Give the position of every Plasmodium parasite and every leukocyte.
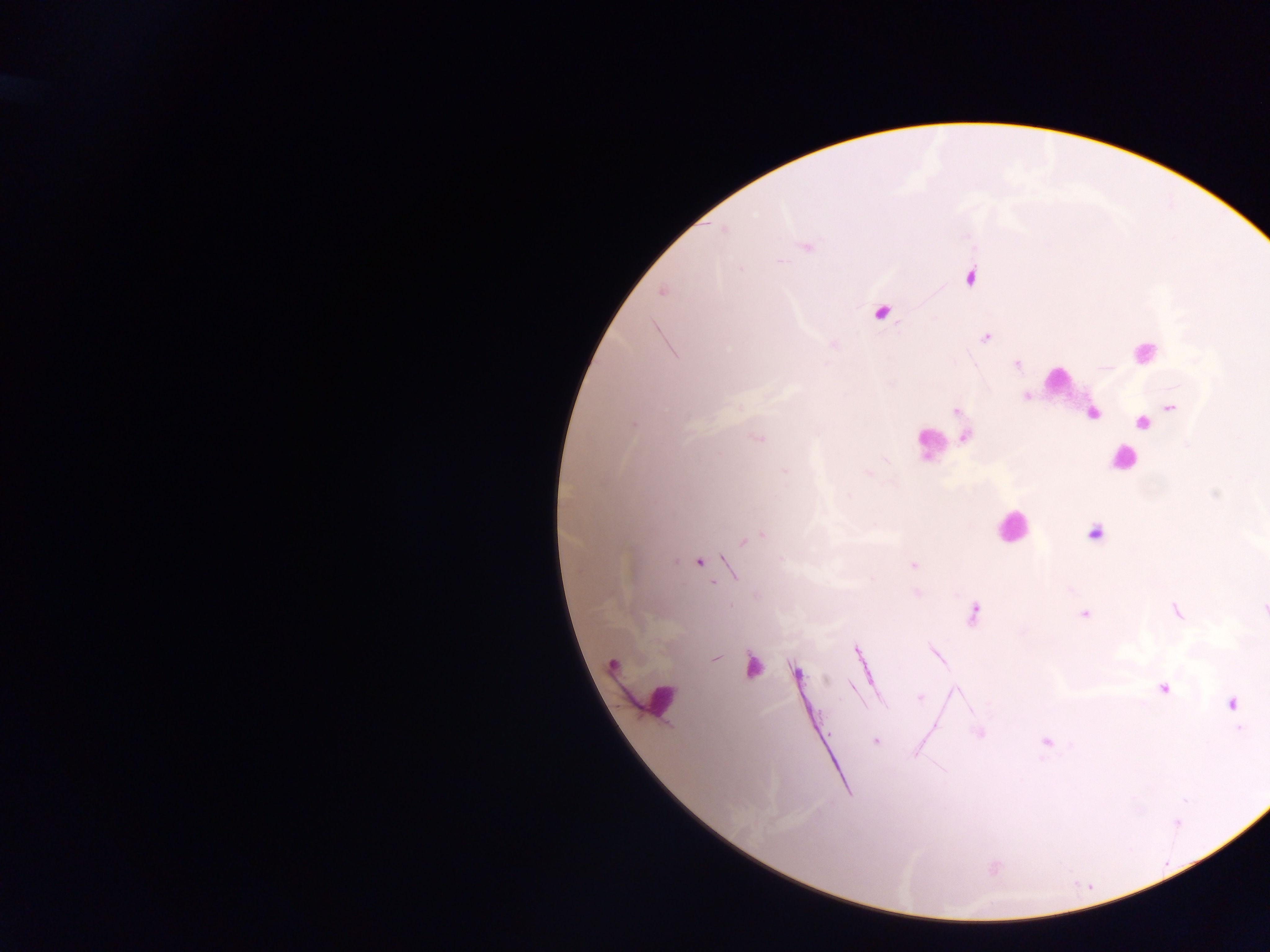

Approximate centers as [x, y] in pixels.
Plasmodium parasites: [724, 229], [807, 247], [778, 261], [969, 278], [662, 291], [986, 338], [1017, 365], [1026, 397], [1171, 407], [956, 411], [1092, 413], [1142, 423], [634, 424], [758, 437], [965, 437], [785, 471], [868, 473], [848, 496], [1095, 534], [758, 535], [749, 539], [699, 562], [913, 565], [917, 593], [1263, 608], [1176, 611], [1085, 613], [973, 614], [936, 654], [716, 658], [613, 664], [797, 672], [1163, 689], [921, 698], [1232, 704], [979, 732], [874, 741], [1046, 742], [994, 867].
Leukocytes: [880, 312], [1143, 352], [1058, 379], [935, 443], [1123, 460], [1012, 527], [753, 663], [657, 700].

preparation = thick blood smear
capture = mobile-phone photograph through a microscope
country = Ghana
image size = 1270×952 pixels
field of view = single